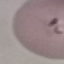 Malaria status: parasitized. Acquired by smartphone through the microscope eyepiece. Giemsa stain. Automatically extracted cell patch, resized to 64 × 64 pixels. Thin blood smear.